Describe the morphology of the erythrocytes.
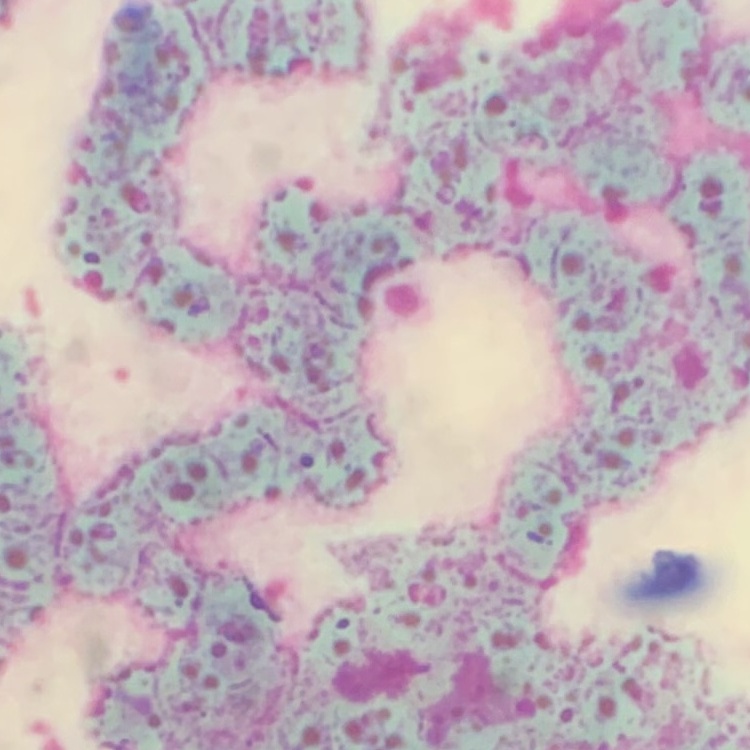

Rouleaux formation.

image type = one tile cut from a larger photomicrograph
stain = Field's or Giemsa
preparation = thin peripheral smear